Give the position of every malaria parasite.
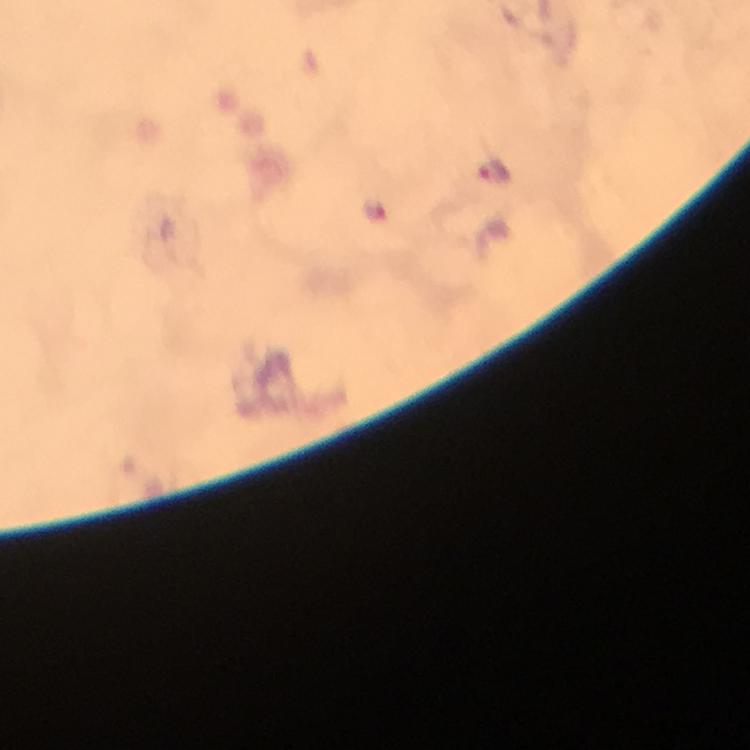
Approximate centers as (x, y) in pixels.
Malaria parasites: (493, 168), (373, 210).

Summary:
  - Immersion oil: applied
  - Magnification: 100x
  - Cropped from: one field of view
  - Capture: smartphone photograph through a microscope
  - Image size: 750×750 pixels
  - Context: from a malaria diagnostic workup
  - Preparation: thick smear
  - Stain: Giemsa